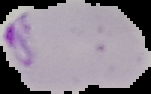

malaria status = parasitized
image size = 151×94 pixels
image type = cell region segmented out of the field of view; surrounding area masked to black
preparation = thin blood film